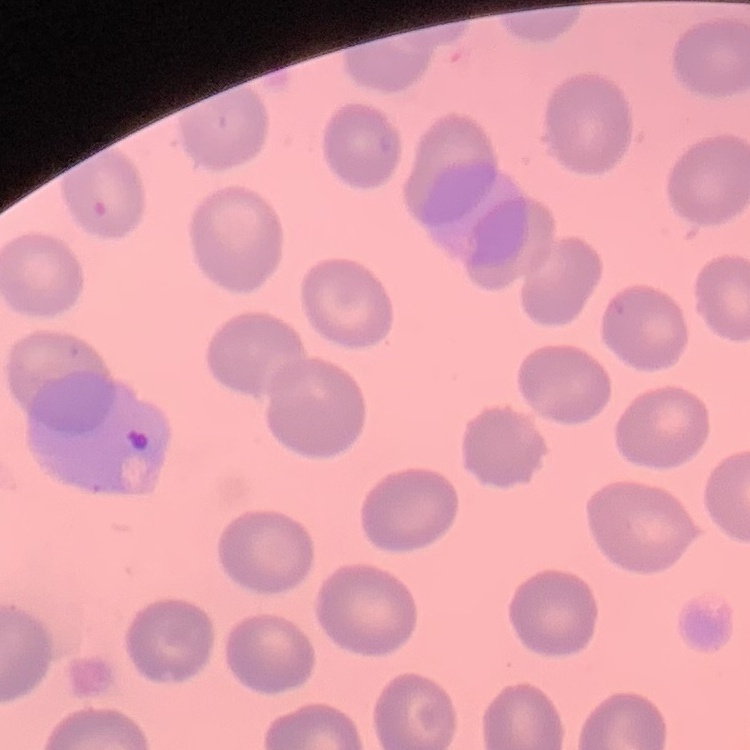

erythrocyte morphology = no rouleaux formation
image type = square crop of a larger photomicrograph
stain = Field's or Giemsa
preparation = thin peripheral smear